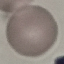 Malaria status: uninfected. Acquired by smartphone through the microscope eyepiece. Automatically extracted cell patch, resized to 64 × 64 pixels. Thin blood film. Giemsa-stained preparation.